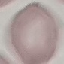
Summary:
  - Result: no malaria parasites seen
  - Preparation: thin blood smear
  - Capture: smartphone through the microscope eyepiece
  - Stain: Giemsa
  - Image type: automatically extracted cell patch, resized to 64 × 64 pixels